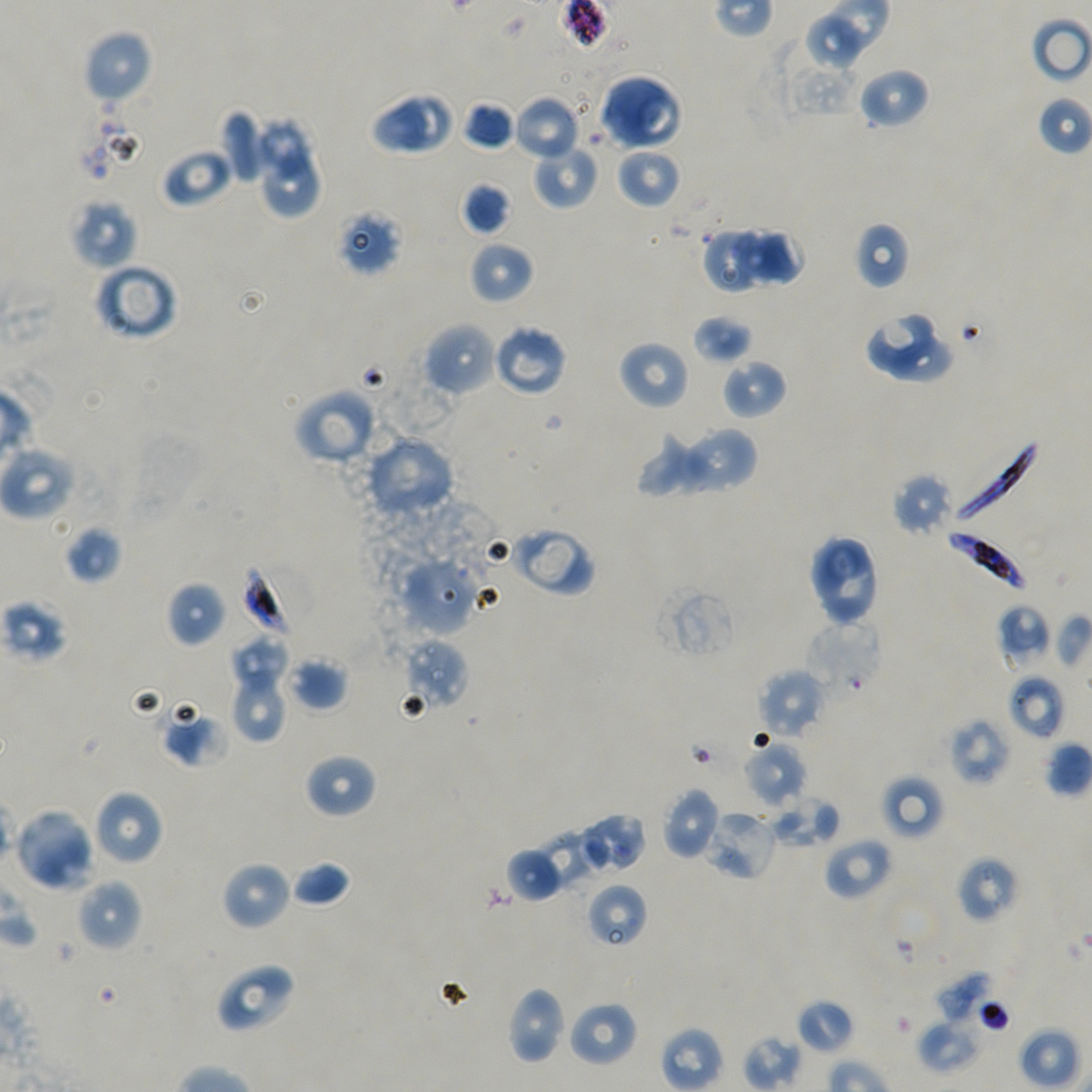
Approximate bounding rectangles given as corner coordinates in pixels from the top-left. Not every red blood cell is marked. Locations of red blood cells of indeterminate infection status: (x1=335, y1=208, x2=401, y2=276), (x1=240, y1=560, x2=314, y2=640), (x1=804, y1=620, x2=884, y2=697), (x1=704, y1=809, x2=778, y2=881), (x1=956, y1=856, x2=1021, y2=923), (x1=585, y1=882, x2=649, y2=948), (x1=962, y1=996, x2=1010, y2=1032). Locations of uninfected red blood cells: (x1=805, y1=12, x2=869, y2=70), (x1=1031, y1=16, x2=1092, y2=84), (x1=83, y1=29, x2=153, y2=105), (x1=858, y1=67, x2=929, y2=129), (x1=598, y1=73, x2=682, y2=151), (x1=371, y1=90, x2=429, y2=154), (x1=397, y1=90, x2=456, y2=151), (x1=1036, y1=94, x2=1092, y2=156), (x1=513, y1=95, x2=581, y2=162), (x1=461, y1=101, x2=515, y2=151), (x1=219, y1=109, x2=264, y2=184), (x1=254, y1=117, x2=314, y2=177), (x1=532, y1=143, x2=600, y2=209), (x1=160, y1=147, x2=233, y2=208), (x1=615, y1=147, x2=682, y2=208), (x1=263, y1=156, x2=323, y2=220), (x1=461, y1=181, x2=511, y2=236), (x1=70, y1=198, x2=138, y2=270), (x1=854, y1=221, x2=911, y2=289), (x1=702, y1=228, x2=758, y2=291), (x1=730, y1=228, x2=803, y2=289), (x1=469, y1=240, x2=534, y2=304), (x1=94, y1=262, x2=179, y2=341), (x1=863, y1=310, x2=939, y2=373), (x1=692, y1=314, x2=752, y2=365), (x1=422, y1=321, x2=498, y2=397), (x1=491, y1=324, x2=568, y2=397), (x1=891, y1=338, x2=956, y2=384), (x1=618, y1=340, x2=690, y2=411), (x1=721, y1=357, x2=787, y2=420), (x1=293, y1=387, x2=378, y2=466), (x1=678, y1=425, x2=759, y2=494), (x1=638, y1=427, x2=719, y2=496), (x1=363, y1=435, x2=455, y2=520), (x1=0, y1=444, x2=75, y2=520), (x1=892, y1=472, x2=954, y2=536), (x1=62, y1=525, x2=122, y2=583), (x1=511, y1=525, x2=595, y2=597), (x1=807, y1=534, x2=881, y2=626), (x1=399, y1=556, x2=477, y2=636), (x1=166, y1=581, x2=226, y2=647), (x1=652, y1=583, x2=740, y2=662), (x1=0, y1=598, x2=68, y2=664), (x1=997, y1=604, x2=1053, y2=668), (x1=1053, y1=613, x2=1092, y2=669), (x1=231, y1=635, x2=287, y2=687), (x1=403, y1=637, x2=469, y2=711), (x1=285, y1=656, x2=349, y2=712), (x1=228, y1=667, x2=288, y2=743), (x1=757, y1=669, x2=826, y2=740), (x1=1008, y1=674, x2=1066, y2=740), (x1=160, y1=708, x2=228, y2=768), (x1=948, y1=717, x2=1011, y2=786), (x1=743, y1=740, x2=807, y2=808), (x1=1044, y1=741, x2=1091, y2=797), (x1=304, y1=753, x2=378, y2=818), (x1=881, y1=774, x2=945, y2=840), (x1=661, y1=788, x2=722, y2=861), (x1=92, y1=789, x2=164, y2=866), (x1=769, y1=793, x2=839, y2=850), (x1=13, y1=807, x2=96, y2=892), (x1=573, y1=812, x2=647, y2=875), (x1=536, y1=830, x2=609, y2=894), (x1=824, y1=837, x2=894, y2=901), (x1=505, y1=846, x2=564, y2=903), (x1=221, y1=860, x2=291, y2=930), (x1=290, y1=860, x2=352, y2=907), (x1=77, y1=878, x2=143, y2=950), (x1=214, y1=962, x2=296, y2=1034), (x1=934, y1=972, x2=995, y2=1025), (x1=505, y1=986, x2=566, y2=1065), (x1=796, y1=998, x2=855, y2=1054), (x1=567, y1=1000, x2=639, y2=1068), (x1=917, y1=1019, x2=980, y2=1072), (x1=660, y1=1026, x2=725, y2=1092), (x1=1018, y1=1027, x2=1080, y2=1090). Locations of infected red blood cells: (x1=950, y1=437, x2=1041, y2=529), (x1=944, y1=530, x2=1024, y2=591). Giemsa-stained preparation. Static in-vitro culture of P. falciparum strain NF54. Blood group of the donor: A+/O+. Image is 1092×1092 pixels. 100x objective under oil immersion, numerical aperture 1.45. Thin blood smear. Single field of view.